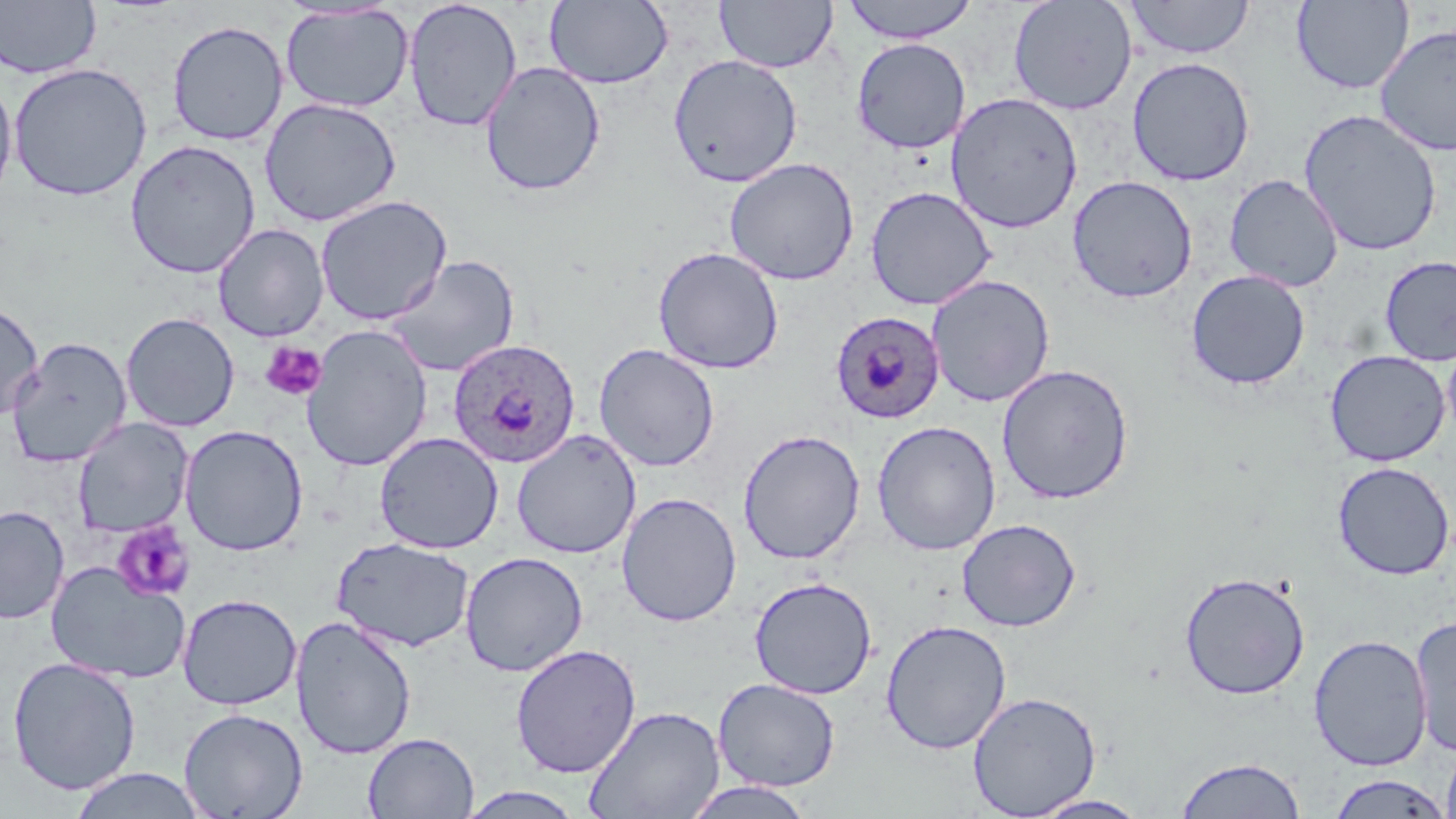

Approximate bounding boxes as (x1, y1, x2, y2) in pixels. Uninfected red blood cell locations: (0, 0, 101, 79), (402, 0, 523, 132), (544, 0, 674, 89), (714, 0, 838, 74), (840, 0, 980, 44), (1008, 0, 1138, 115), (1125, 0, 1255, 59), (1291, 0, 1415, 94), (280, 3, 415, 114), (167, 20, 288, 146), (1374, 22, 1455, 157), (851, 37, 971, 154), (667, 54, 803, 188), (1127, 56, 1256, 186), (480, 61, 606, 197), (8, 63, 152, 201), (0, 74, 18, 207), (946, 91, 1083, 234), (259, 97, 402, 227), (1298, 109, 1443, 257), (125, 139, 261, 279), (724, 157, 859, 286), (1224, 174, 1344, 293), (1068, 175, 1198, 304), (865, 186, 996, 310), (315, 195, 453, 326), (213, 223, 329, 342), (653, 246, 784, 374), (385, 255, 520, 378), (1379, 255, 1456, 366), (1186, 269, 1310, 390), (926, 274, 1055, 407), (0, 302, 43, 422), (121, 311, 239, 432), (301, 323, 433, 472), (7, 337, 132, 468), (1442, 337, 1456, 445), (593, 343, 720, 472), (1324, 349, 1450, 467), (996, 363, 1134, 504), (73, 418, 193, 537), (871, 420, 1002, 556), (179, 425, 308, 556), (511, 428, 641, 559), (737, 428, 866, 564), (374, 431, 504, 554), (1332, 461, 1454, 580), (616, 492, 742, 627), (0, 505, 69, 624), (956, 518, 1081, 632), (331, 537, 476, 652), (459, 551, 588, 676), (45, 560, 192, 685), (1178, 570, 1311, 700), (749, 576, 877, 699), (177, 593, 302, 710), (1410, 613, 1456, 757), (291, 614, 417, 760), (880, 619, 1012, 754), (1308, 633, 1432, 772), (510, 643, 641, 778), (7, 656, 141, 795), (713, 678, 840, 792), (967, 690, 1102, 818), (583, 704, 725, 819), (178, 707, 308, 819), (363, 732, 479, 818), (1442, 742, 1456, 819), (1175, 756, 1306, 818), (68, 768, 208, 818), (1324, 773, 1454, 818), (678, 780, 818, 819), (452, 786, 589, 818), (1026, 794, 1152, 818). Plasmodium ovale-infected red blood cell locations: (829, 310, 946, 424), (448, 337, 581, 468). Platelet locations: (260, 341, 327, 402), (111, 522, 196, 602). Slide-level diagnosis: Plasmodium ovale. Single field of view. May-Grünwald-Giemsa-stained preparation. Optical microscopy. Thin blood smear. Image is 1456×819 pixels. Captured at 1000x magnification.